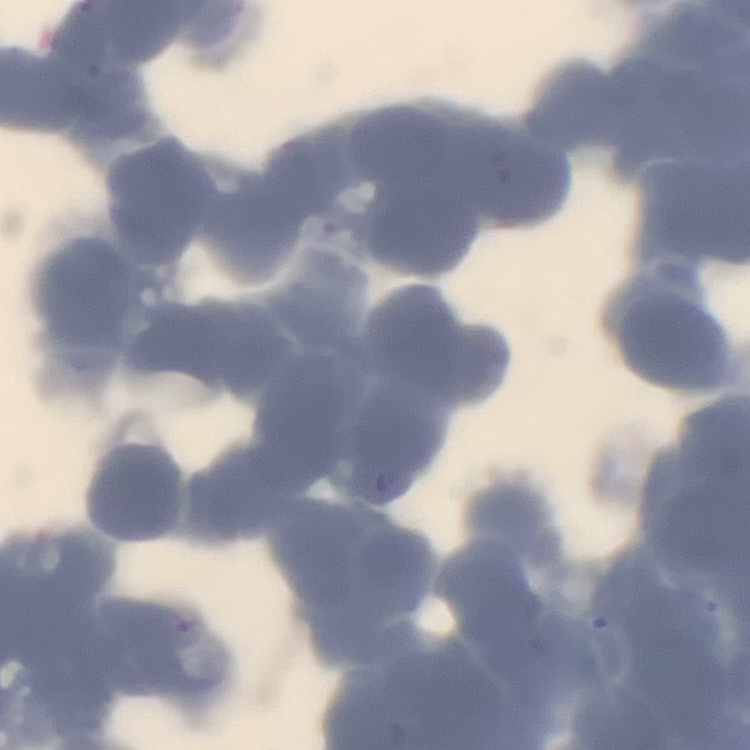

The erythrocytes exhibit rouleaux formation. Field's or Giemsa stain. One tile cut from a larger photomicrograph. Thin blood smear.